State the preparation type.
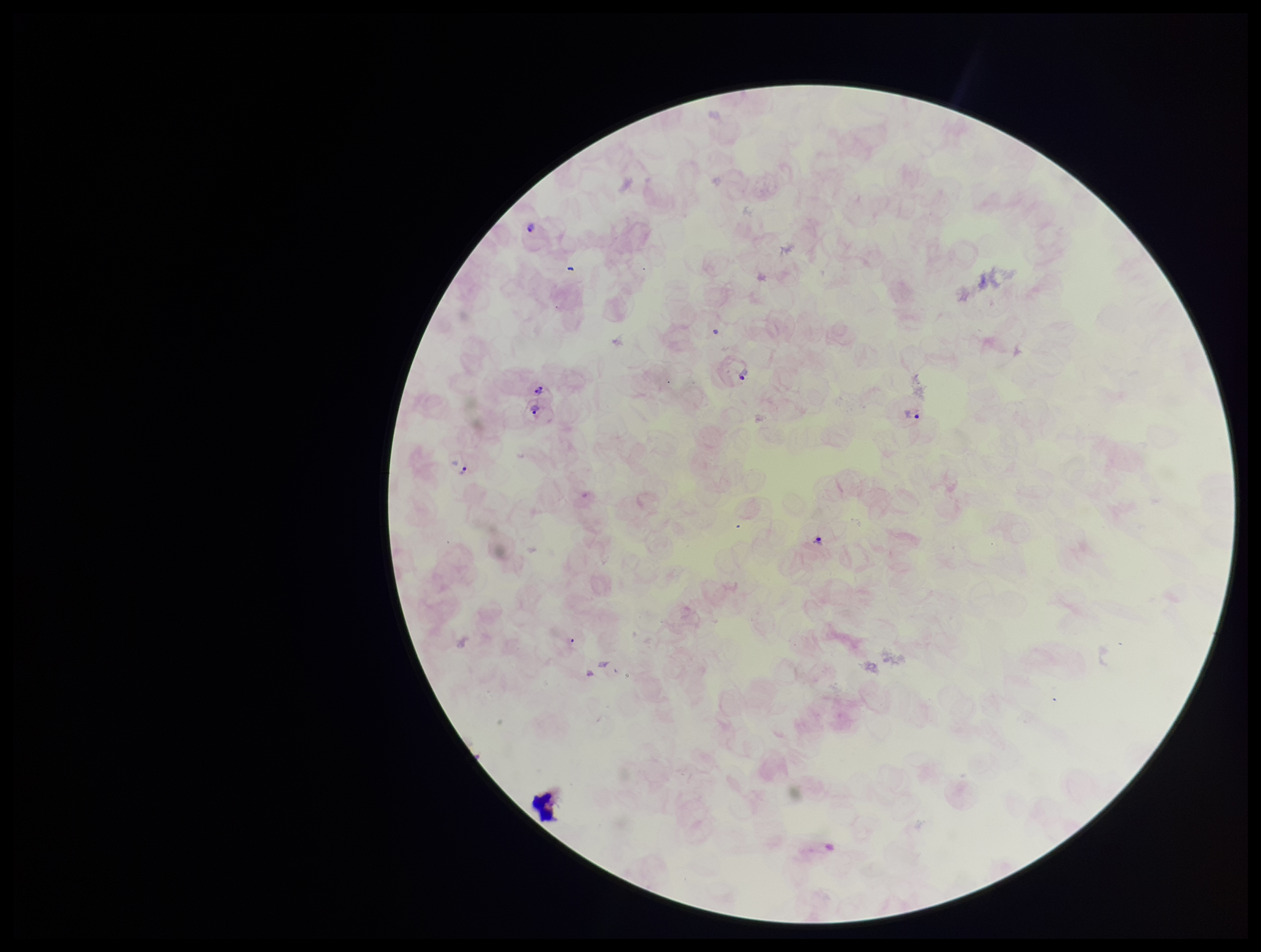
Thick.

leukocyte count = 7
stain = Giemsa
capture = smartphone photograph through the microscope eyepiece
image size = 1261×952 pixels
Plasmodium parasites = identified
field of view = one from this slide
parasite count = 1
patient malaria status = infected
species reported for this patient = Plasmodium vivax